Locate every blood parasite and identify its species.
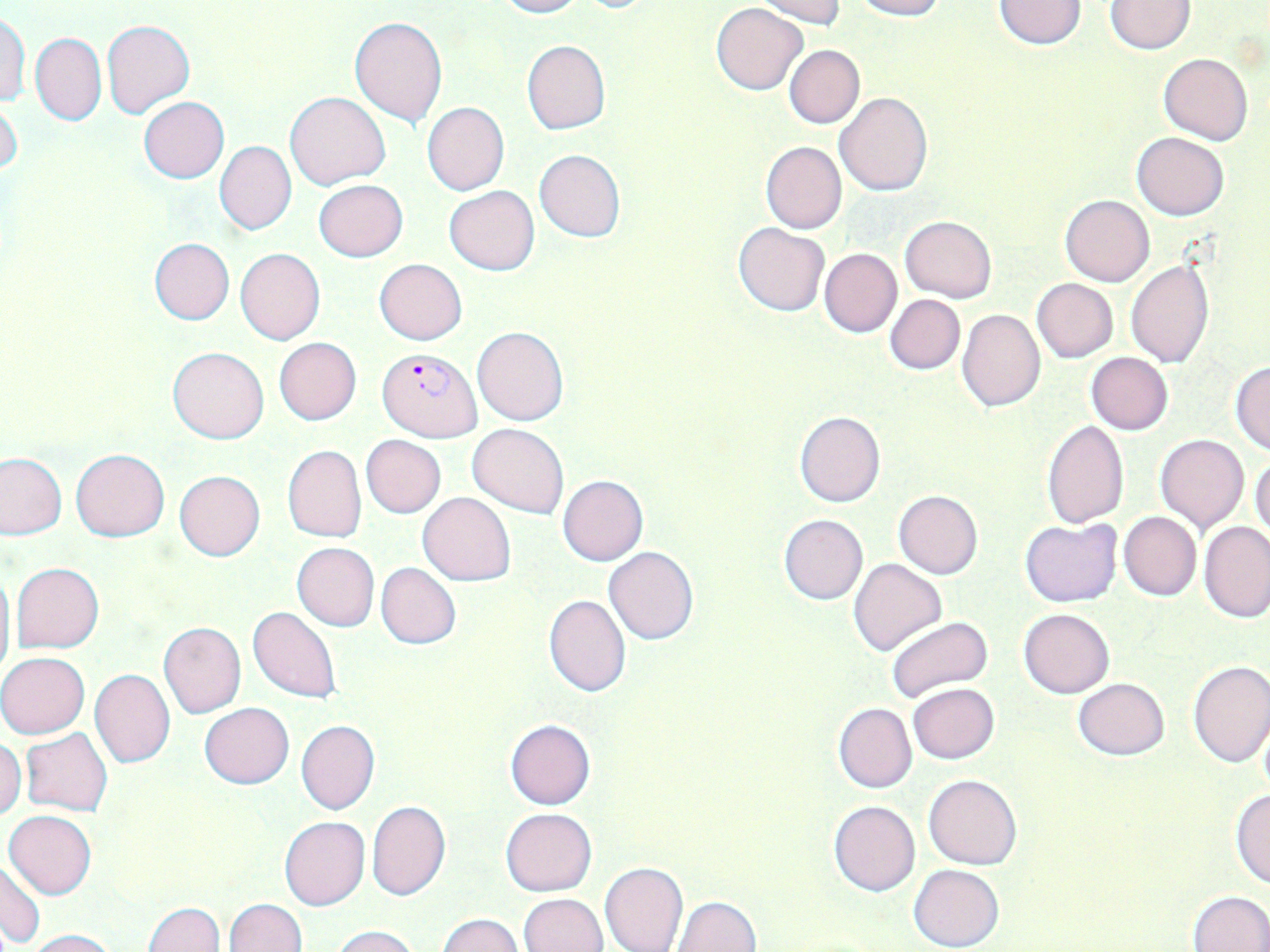
Approximate bounding boxes as (x1, y1, x2, y2) in pixels.
Plasmodium falciparum-infected red blood cells: (378, 348, 483, 442).
No Plasmodium ovale, Plasmodium malariae, Plasmodium vivax, Babesia divergens, or Trypanosoma brucei observed.

slide_level_diagnosis: Plasmodium falciparum
image_size: 1270×952 pixels
field_of_view: one of a larger specimen
modality: light microscopy
preparation: thin blood film
uninfected_red_blood_cell_locations: 'approximate bounding boxes as (x1, y1, x2, y2) in pixels: (494, 0, 584, 18), (753, 0, 846, 27), (850, 0, 945, 20), (992, 0, 1087, 50), (1107, 1, 1194, 53), (711, 2, 808, 96), (0, 10, 31, 107), (350, 14, 448, 126), (102, 20, 194, 118), (30, 32, 106, 126), (522, 40, 609, 135), (783, 45, 864, 128), (1159, 53, 1252, 145), (285, 91, 391, 188), (835, 92, 932, 197), (139, 97, 229, 184), (0, 98, 23, 179), (422, 102, 509, 195), (1133, 132, 1228, 219), (215, 141, 296, 234), (761, 142, 846, 234), (534, 149, 625, 242), (314, 180, 407, 261), (444, 186, 540, 275), (1060, 195, 1155, 286), (900, 215, 997, 302), (733, 222, 829, 316), (149, 238, 235, 325), (235, 247, 325, 344), (819, 248, 902, 337), (374, 259, 467, 344), (1126, 262, 1213, 367), (1032, 278, 1117, 363), (886, 294, 964, 374), (957, 309, 1045, 412), (472, 326, 567, 425), (275, 338, 361, 424), (168, 346, 270, 443), (1086, 352, 1173, 435), (1229, 361, 1270, 453), (794, 411, 886, 507), (1042, 419, 1129, 527), (468, 423, 568, 518), (1156, 434, 1249, 533), (360, 435, 445, 517), (281, 445, 365, 542), (72, 449, 170, 541), (0, 451, 66, 539), (1250, 455, 1270, 541), (174, 471, 265, 562), (558, 475, 648, 565), (893, 490, 984, 579), (418, 493, 515, 585), (1119, 511, 1202, 601), (779, 514, 868, 605), (1020, 518, 1122, 607), (1199, 521, 1269, 624), (292, 542, 379, 631), (603, 547, 700, 645), (849, 559, 947, 656), (11, 562, 105, 652), (376, 563, 461, 649), (0, 564, 15, 683), (570, 568, 681, 675), (543, 595, 632, 697), (248, 606, 342, 704), (1019, 608, 1114, 698), (885, 616, 994, 704), (158, 622, 246, 718), (0, 653, 89, 738), (1187, 659, 1270, 768), (89, 670, 175, 768), (1073, 677, 1170, 760), (908, 683, 1000, 765), (199, 702, 294, 788), (834, 702, 917, 793), (1257, 717, 1270, 799), (504, 719, 596, 809), (297, 720, 379, 814), (21, 728, 112, 816), (0, 739, 26, 819), (925, 774, 1021, 869), (1230, 787, 1270, 889), (367, 801, 450, 901), (828, 801, 921, 896), (500, 808, 597, 896), (4, 809, 97, 898), (279, 816, 369, 910), (0, 859, 45, 948), (599, 862, 687, 952), (909, 864, 1003, 951), (1186, 891, 1270, 952), (520, 893, 608, 952), (674, 896, 760, 952), (224, 898, 305, 952), (144, 903, 224, 952), (438, 914, 522, 952), (331, 925, 421, 952), (25, 928, 117, 952)'
stain: May-Grünwald-Giemsa
magnification: 1000x